Locate every Plasmodium falciparum-infected red blood cell.
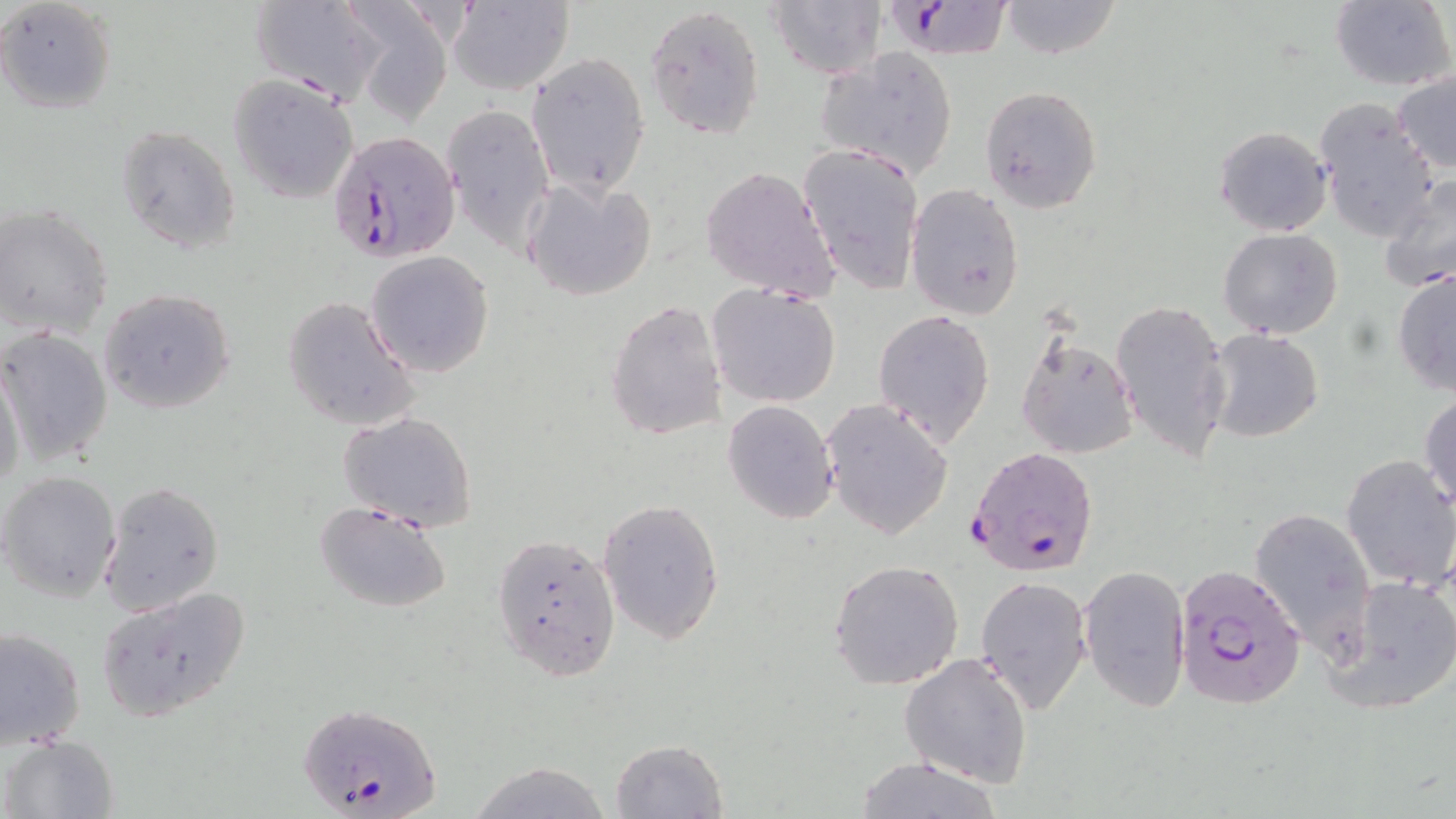
Approximate bounding boxes as (x1,y1)-(x2,y2) corner pairs in pixels.
Plasmodium falciparum-infected red blood cells: (875,1)-(1018,62), (327,129)-(461,259), (966,447)-(1099,579), (1176,565)-(1306,710), (298,701)-(439,819).

Summary:
  - Uninfected red blood cell locations: (0,0)-(117,113), (248,0)-(386,105), (999,0)-(1121,58), (1331,0)-(1455,90), (448,1)-(573,96), (768,1)-(885,81), (645,4)-(766,141), (350,6)-(454,125), (816,47)-(959,180), (526,53)-(650,195), (1392,71)-(1456,174), (228,74)-(362,203), (979,85)-(1103,212), (1313,101)-(1439,244), (445,103)-(555,257), (113,125)-(242,254), (1213,125)-(1331,236), (801,142)-(925,295), (700,165)-(839,301), (1379,174)-(1456,295), (520,175)-(658,303), (905,182)-(1025,320), (2,205)-(116,339), (1218,228)-(1344,340), (364,251)-(495,377), (1392,268)-(1456,395), (707,284)-(841,408), (99,287)-(237,414), (282,295)-(420,432), (605,297)-(728,441), (1110,299)-(1231,463), (872,309)-(994,445), (0,327)-(114,467), (1205,328)-(1324,443), (1016,329)-(1140,462), (1,359)-(27,494), (1419,393)-(1456,511), (822,399)-(952,541), (722,401)-(838,525), (338,410)-(479,530), (1341,454)-(1456,591), (1,470)-(122,602), (97,480)-(226,617), (597,496)-(726,645), (314,500)-(451,613), (1250,506)-(1377,656), (492,532)-(618,681), (827,558)-(966,688), (1079,564)-(1190,713), (975,574)-(1092,714), (1324,575)-(1456,713), (95,587)-(253,722), (1,626)-(86,751), (900,652)-(1034,789), (3,734)-(117,819), (610,739)-(727,818), (853,756)-(1004,817), (463,762)-(612,819)
  - Slide-level diagnosis: Plasmodium falciparum
  - Magnification: 1000x
  - Preparation: thin blood smear
  - Field of view: one of a larger specimen
  - Stain: May-Grünwald-Giemsa
  - Image size: 1456×819 pixels
  - Modality: light microscopy